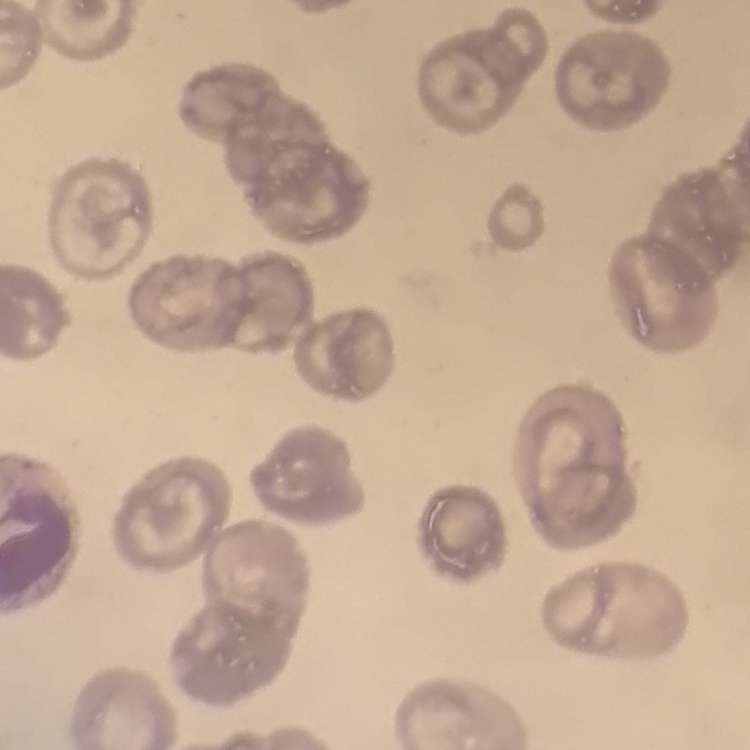

red_blood_cell_morphology: no rouleaux formation
image_type: square crop of a larger photomicrograph
preparation: thin peripheral smear
stain: Field's or Giemsa